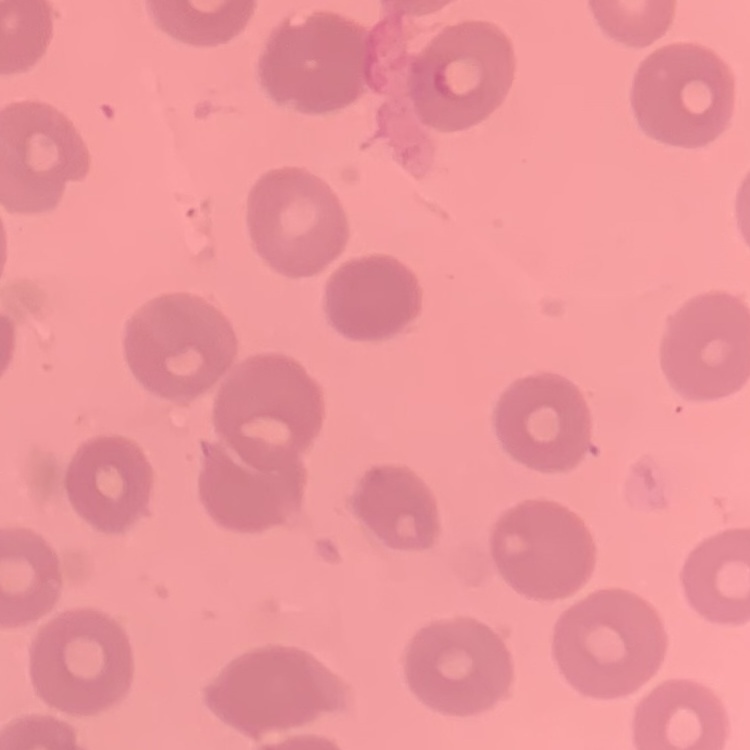

The erythrocytes show no rouleaux formation. Stained with either Field's or Giemsa. Thin blood film. One tile cut from a larger photomicrograph.